Give the preparation type.
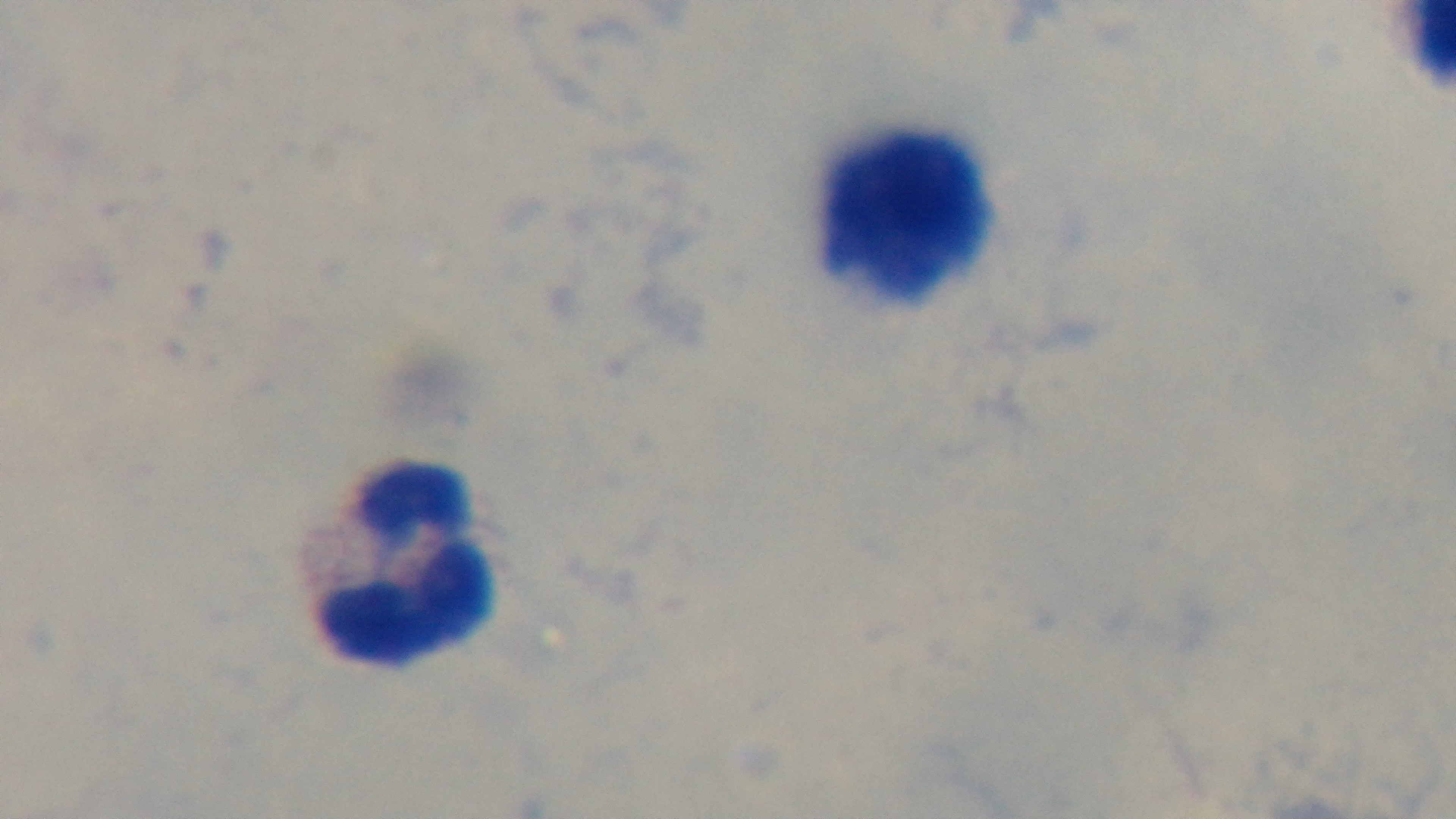

It is a thick blood film.

Single field of view. Giemsa stain. Oil-immersion objective, 100x. Mounted 4K digital camera. Photomicrograph. Malaria status: uninfected.